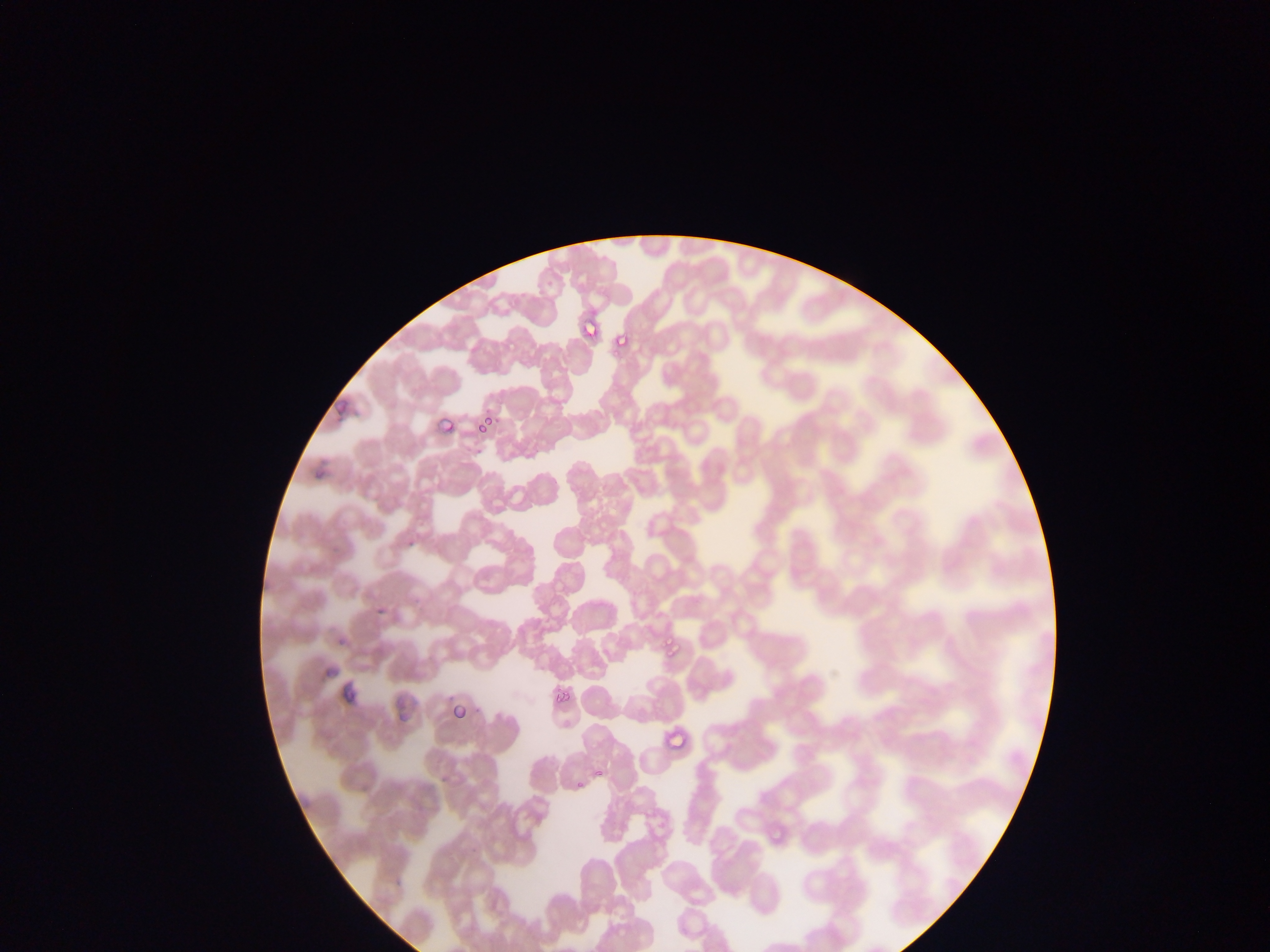

Approximate bounding boxes as (left, top, right, bottom) in pixels. Malaria parasite locations: (579, 310, 604, 333), (605, 337, 629, 357), (476, 416, 496, 433), (430, 421, 452, 440), (466, 440, 483, 459), (308, 463, 331, 480), (403, 515, 424, 545), (371, 606, 392, 627), (334, 630, 350, 649), (663, 643, 681, 674), (549, 681, 584, 710), (450, 700, 476, 719), (666, 721, 689, 752), (590, 764, 608, 784), (570, 772, 587, 795), (766, 828, 795, 848). Thin blood film. Single field of view. Image is 1270×952 pixels. Collected in Ghana. Mobile-phone photograph taken through the microscope.